Report the malaria status of this cell.
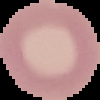
It is uninfected.

Cell region segmented out of the field of view; the surrounding area is masked to black. From a thin blood smear. Image is 100×100 pixels.